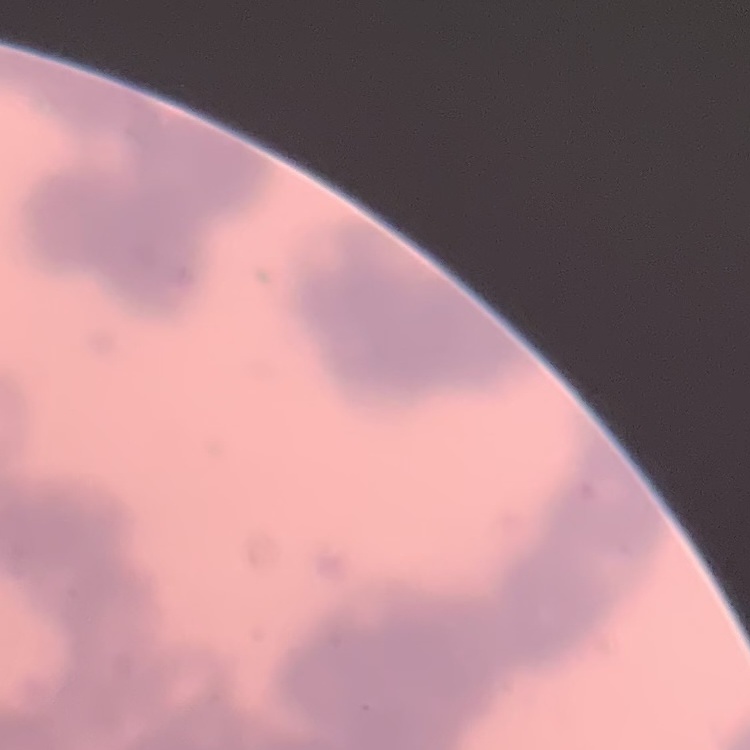
{
  "erythrocyte_morphology": "rouleaux formation",
  "image_type": "one tile cut from a larger photomicrograph",
  "preparation": "thin peripheral smear",
  "stain": "Field's or Giemsa"
}